Outline each blood parasite and name the species.
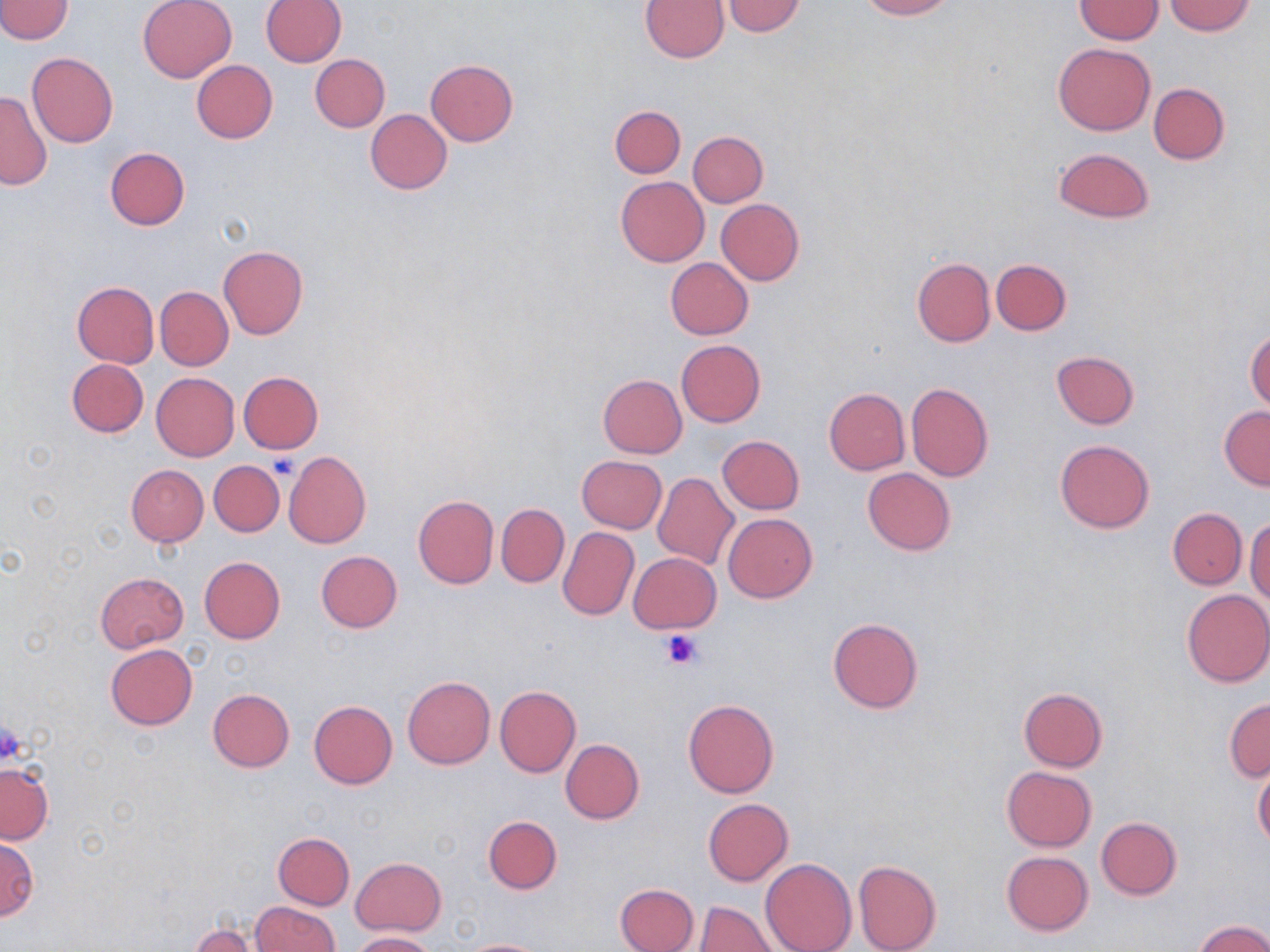

No blood parasites seen.

Summary:
  - Coordinate format: approximate bounding boxes as [x1, y1, x2, y2] in pixels
  - Platelet locations: [269, 453, 301, 479], [659, 628, 705, 670], [0, 719, 26, 766]
  - Uninfected red blood cell locations: [0, 0, 73, 44], [137, 0, 237, 83], [261, 0, 346, 66], [857, 0, 957, 20], [1076, 0, 1162, 44], [641, 1, 729, 62], [722, 1, 807, 36], [1164, 1, 1256, 36], [1053, 43, 1155, 136], [27, 51, 119, 148], [310, 54, 390, 131], [425, 59, 518, 145], [191, 60, 277, 144], [1148, 83, 1229, 164], [0, 90, 51, 190], [610, 104, 685, 178], [366, 109, 452, 195], [688, 131, 768, 208], [105, 147, 189, 229], [1053, 148, 1155, 223], [615, 176, 710, 266], [717, 199, 804, 285], [219, 245, 308, 339], [665, 258, 754, 339], [912, 258, 995, 346], [991, 259, 1071, 335], [71, 281, 159, 367], [156, 287, 233, 370], [1245, 329, 1270, 413], [676, 339, 765, 427], [1052, 351, 1139, 429], [67, 358, 148, 437], [238, 371, 323, 453], [151, 372, 239, 461], [598, 374, 687, 458], [907, 382, 994, 482], [824, 388, 910, 475], [1219, 406, 1270, 489], [718, 435, 804, 514], [1055, 438, 1155, 534], [283, 451, 371, 548], [577, 455, 666, 533], [209, 460, 285, 537], [126, 464, 208, 546], [863, 468, 955, 556], [654, 473, 738, 569], [413, 494, 498, 588], [497, 502, 568, 588], [1168, 508, 1246, 589], [723, 513, 817, 602], [1246, 518, 1270, 604], [558, 526, 638, 620], [316, 550, 403, 632], [630, 552, 720, 634], [199, 556, 285, 643], [95, 572, 189, 653], [1182, 589, 1270, 688], [828, 618, 924, 713], [106, 644, 198, 730], [402, 676, 494, 770], [495, 686, 581, 777], [208, 688, 294, 772], [1019, 688, 1108, 771], [1224, 698, 1270, 781], [309, 699, 397, 788], [683, 699, 778, 797], [560, 739, 644, 825], [0, 764, 52, 844], [1002, 765, 1096, 851], [1254, 765, 1270, 850], [704, 798, 793, 885], [483, 815, 562, 894], [1096, 818, 1182, 900], [273, 832, 354, 909], [0, 834, 37, 921], [1002, 851, 1094, 936], [352, 857, 445, 935], [761, 857, 856, 952], [853, 859, 941, 952], [614, 882, 698, 952], [695, 900, 777, 951], [252, 901, 337, 952], [1196, 920, 1270, 952], [190, 921, 266, 951], [350, 931, 435, 951], [458, 937, 551, 952]
  - Slide-level diagnosis: negative for blood parasites
  - Preparation: thin blood film
  - Field of view: single
  - Magnification: 1000x
  - Modality: light microscopy
  - Image size: 1270×952 pixels
  - Stain: May-Grünwald-Giemsa